Assess this cell for malaria.
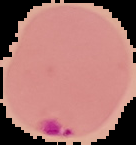

Parasitized.

{
  "image_size": "136×145 pixels",
  "image_type": "segmented cell region with the area outside set to black",
  "preparation": "thin blood smear"
}